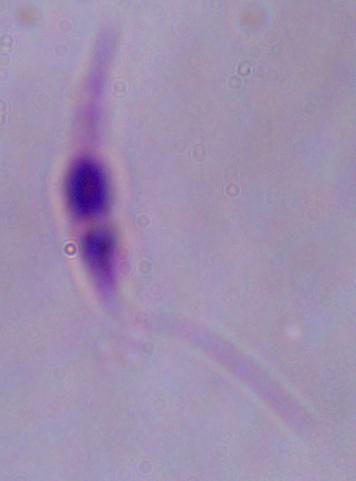

Summary:
  - Magnification: 1000x
  - Identification: Leishmania
  - Modality: photomicrograph